Locate every Babesia divergens-infected red blood cell.
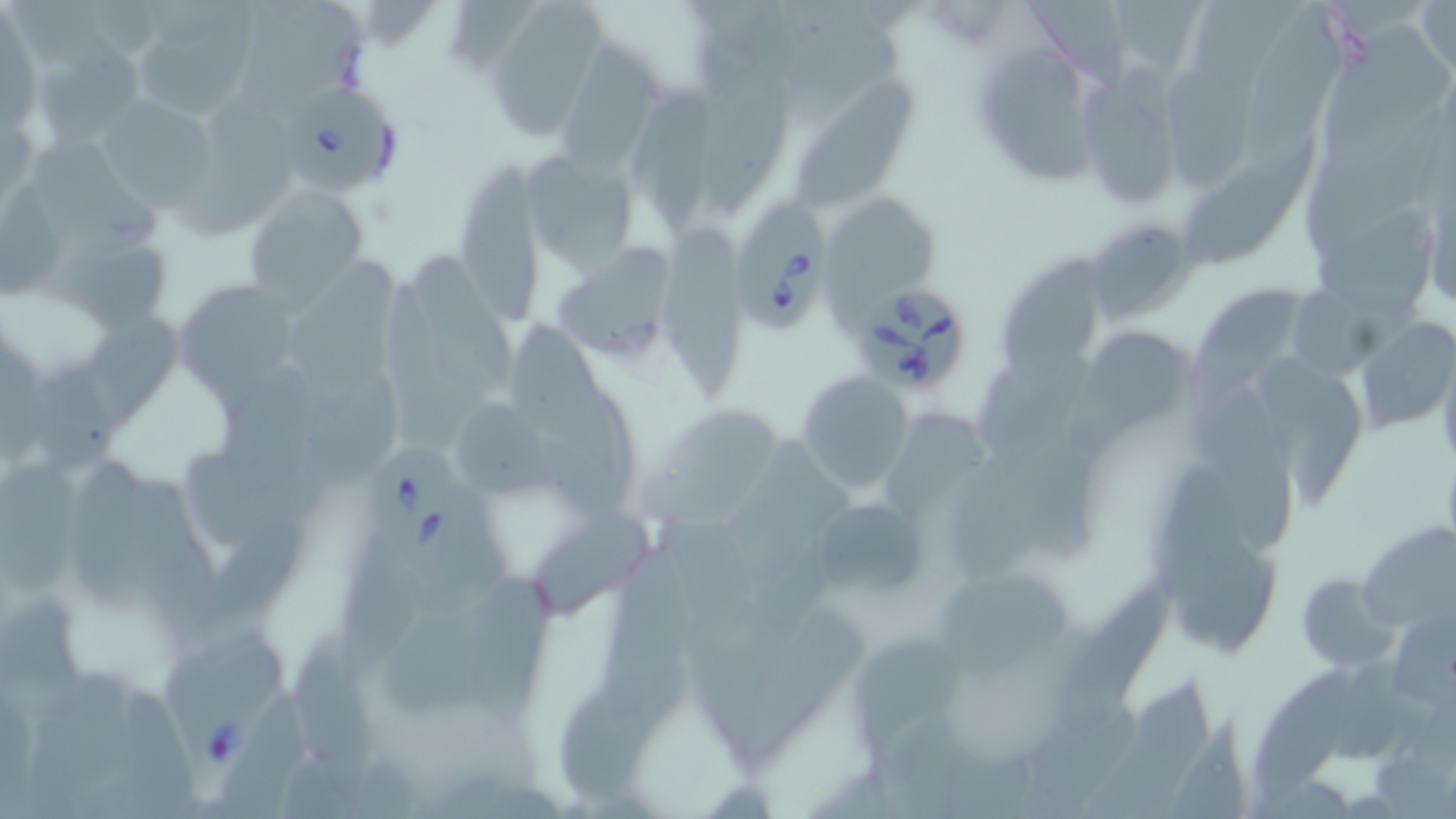
Approximate bounding boxes as (x1, y1, x2, y2) in pixels.
Babesia divergens-infected red blood cells: (285, 85, 402, 192), (731, 205, 829, 335), (862, 288, 966, 394), (365, 439, 473, 571), (156, 621, 293, 775).

Uninfected red blood cell locations: (489, 0, 610, 139), (1197, 0, 1303, 80), (243, 1, 368, 118), (789, 1, 885, 66), (1024, 1, 1125, 88), (1116, 1, 1201, 70), (1417, 1, 1455, 78), (140, 2, 260, 125), (1242, 3, 1356, 186), (1324, 23, 1456, 168), (783, 34, 905, 129), (559, 36, 658, 196), (977, 37, 1097, 187), (35, 38, 152, 145), (704, 58, 794, 218), (1169, 62, 1259, 192), (1085, 65, 1191, 209), (791, 75, 929, 206), (629, 78, 718, 239), (184, 92, 301, 236), (102, 95, 212, 212), (1303, 109, 1446, 264), (25, 137, 170, 262), (1180, 137, 1326, 266), (523, 149, 639, 270), (460, 161, 543, 328), (245, 189, 371, 311), (1311, 203, 1441, 316), (1086, 217, 1200, 326), (663, 221, 754, 399), (48, 248, 174, 338), (556, 249, 679, 361), (416, 251, 521, 400), (1005, 251, 1109, 399), (285, 255, 397, 414), (1196, 277, 1308, 414), (176, 279, 299, 411), (1285, 286, 1428, 382), (85, 313, 195, 429), (502, 313, 620, 468), (1355, 315, 1456, 438), (1068, 334, 1189, 469), (1265, 355, 1366, 509), (36, 367, 121, 473), (293, 368, 401, 482), (794, 372, 915, 491), (979, 373, 1076, 476), (1192, 388, 1298, 555), (539, 398, 638, 519), (457, 401, 555, 498), (640, 404, 778, 533), (885, 412, 991, 518), (732, 435, 860, 578), (951, 448, 1046, 586), (71, 452, 153, 627), (1004, 453, 1100, 560), (1, 461, 88, 598), (1160, 470, 1245, 601), (114, 475, 218, 626), (805, 494, 926, 602), (533, 505, 648, 625), (204, 511, 318, 638), (656, 517, 759, 643), (1358, 521, 1455, 634), (336, 535, 419, 681), (600, 548, 686, 721), (941, 567, 1078, 676), (1295, 571, 1398, 671), (464, 572, 557, 733), (1054, 582, 1182, 739), (1, 590, 85, 702), (386, 604, 495, 714), (740, 607, 877, 767), (1392, 614, 1456, 714), (296, 629, 374, 798), (849, 636, 965, 763), (1339, 659, 1415, 758), (33, 662, 138, 800), (1252, 666, 1356, 803), (1090, 675, 1219, 819), (558, 676, 682, 802), (224, 690, 308, 818), (1017, 706, 1140, 819), (1170, 714, 1255, 819). Slide-level diagnosis: Babesia divergens. Captured at 1000x magnification. Single field of view. May-Grünwald-Giemsa-stained preparation. Image is 1456×819 pixels. Thin blood film. Light microscopy.